Locate and identify every blood parasite.
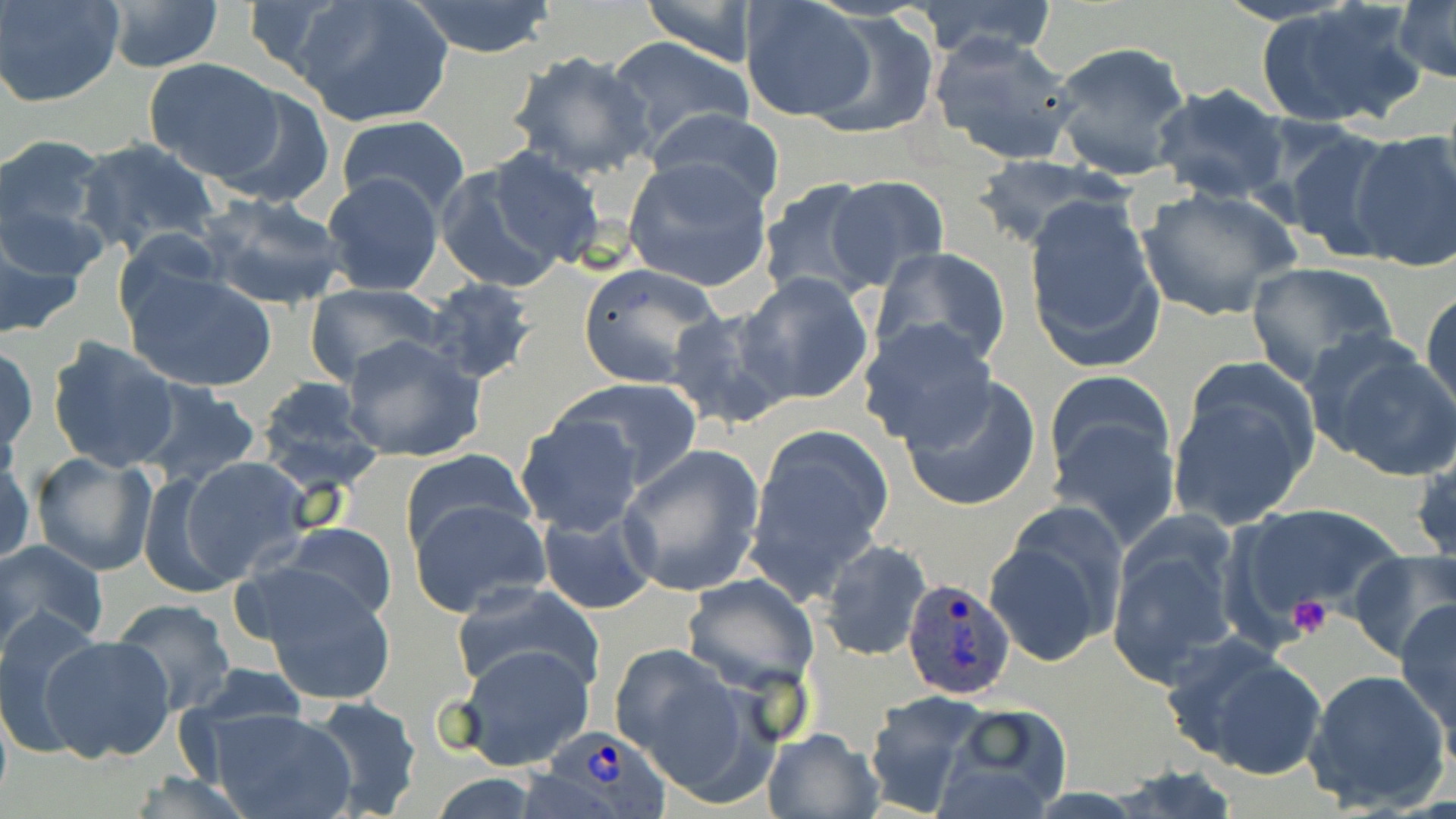

Approximate bounding boxes as (x1, y1, x2, y2) in pixels.
Plasmodium ovale-infected red blood cells: (901, 578, 1016, 700), (544, 724, 673, 819).
No Plasmodium falciparum, Plasmodium malariae, Plasmodium vivax, Babesia divergens, or Trypanosoma brucei observed.

Uninfected red blood cell locations: (0, 0, 125, 107), (101, 0, 226, 73), (292, 0, 453, 127), (637, 0, 761, 66), (912, 0, 1062, 63), (403, 1, 560, 58), (738, 1, 875, 125), (1258, 2, 1425, 129), (1392, 2, 1456, 82), (806, 11, 939, 139), (931, 31, 1080, 164), (605, 37, 754, 147), (1049, 41, 1193, 182), (507, 50, 656, 180), (143, 58, 284, 182), (1148, 83, 1292, 204), (213, 84, 336, 207), (647, 107, 787, 213), (335, 114, 472, 219), (1278, 123, 1400, 261), (1345, 128, 1456, 274), (0, 135, 110, 252), (73, 138, 223, 259), (437, 153, 597, 290), (967, 156, 1126, 245), (622, 159, 774, 294), (320, 172, 446, 296), (823, 174, 950, 290), (757, 177, 886, 305), (1136, 185, 1302, 323), (1022, 190, 1165, 372), (196, 192, 349, 311), (0, 212, 89, 343), (871, 247, 1012, 370), (1244, 261, 1398, 387), (576, 262, 724, 388), (122, 264, 279, 393), (738, 273, 874, 405), (419, 278, 541, 386), (302, 283, 446, 389), (1422, 286, 1455, 426), (665, 303, 796, 432), (859, 318, 997, 451), (44, 334, 183, 473), (340, 335, 487, 460), (1306, 337, 1456, 480), (1, 342, 38, 460), (1165, 362, 1320, 532), (1046, 370, 1177, 548), (901, 375, 1041, 514), (253, 377, 386, 498), (553, 377, 703, 491), (135, 380, 266, 493), (514, 411, 645, 537), (743, 425, 895, 605), (1414, 442, 1455, 576), (616, 445, 766, 597), (398, 449, 531, 553), (0, 451, 34, 567), (32, 451, 160, 575), (173, 453, 315, 586), (409, 497, 552, 618), (1234, 503, 1403, 627), (535, 509, 659, 614), (984, 512, 1124, 670), (1104, 516, 1247, 689), (271, 523, 397, 626), (819, 538, 934, 662), (0, 539, 109, 650), (1348, 548, 1456, 664), (243, 566, 398, 705), (681, 573, 819, 693), (450, 583, 605, 699), (110, 597, 238, 716), (1396, 599, 1456, 743), (0, 609, 104, 757), (37, 632, 175, 763), (1165, 635, 1330, 782), (455, 643, 596, 771), (609, 644, 761, 800), (1302, 668, 1451, 812), (863, 692, 993, 815), (302, 696, 424, 819), (194, 704, 361, 819), (932, 704, 1075, 819), (761, 728, 882, 819), (1109, 763, 1244, 819), (120, 772, 263, 819). Platelet locations: (1287, 596, 1335, 640). Slide-level diagnosis: Plasmodium ovale. One field of a larger specimen. Image is 1456×819 pixels. Light microscopy. Captured at 1000x magnification. Thin blood film. May-Grünwald-Giemsa-stained preparation.